Point out each leukocyte.
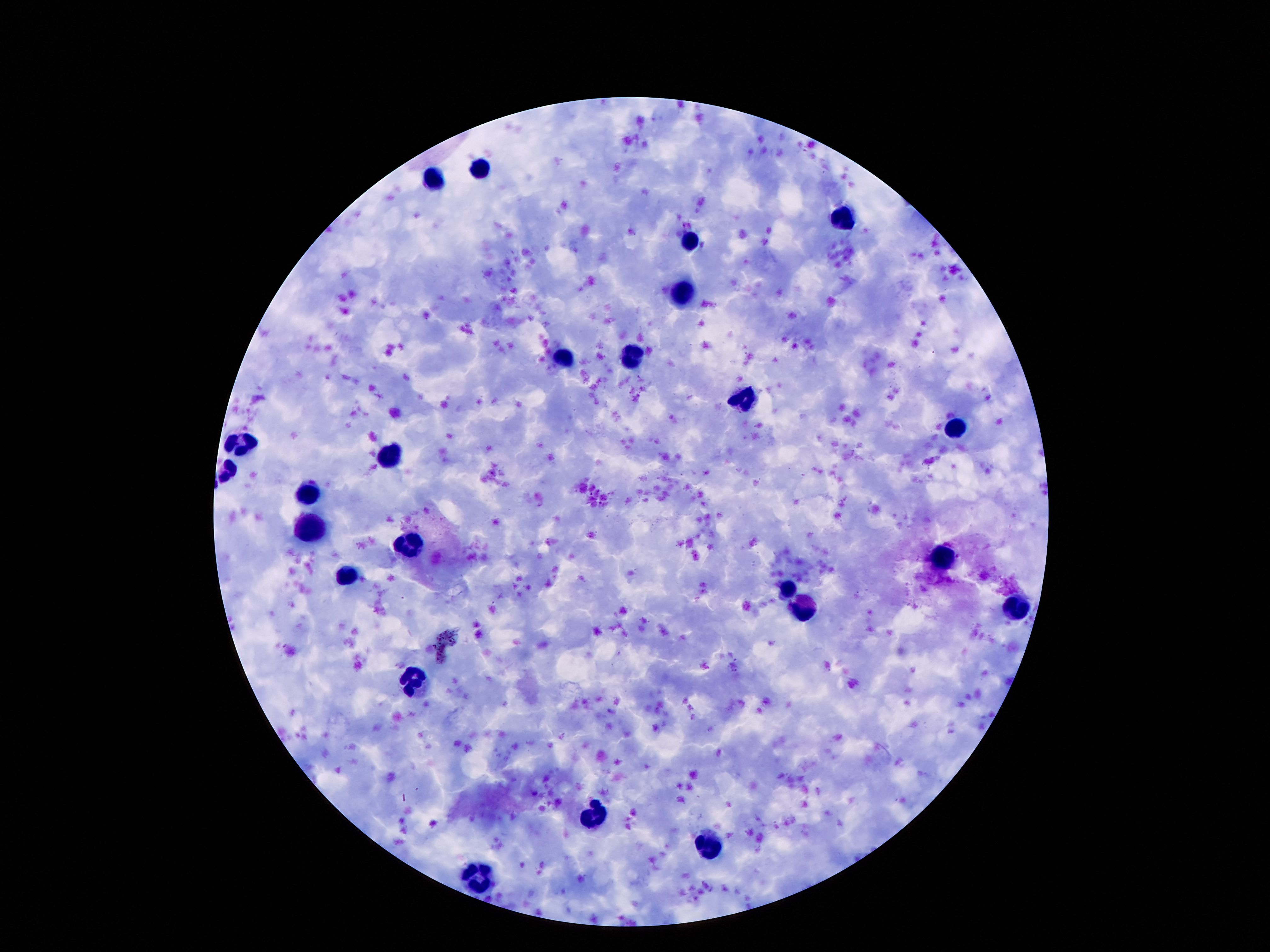
Approximate centers as [x, y] in pixels.
Leukocytes: [483, 167], [433, 181], [843, 219], [692, 241], [680, 292], [635, 355], [562, 358], [744, 400], [957, 430], [244, 444], [392, 459], [304, 494], [310, 528], [412, 544], [944, 555], [346, 576], [787, 589], [805, 607], [1018, 609], [412, 679], [592, 816], [714, 844], [481, 878].

Summary:
  - Image size: 1270×952 pixels
  - Magnification: 100x
  - Field of view: single
  - Stain: Giemsa
  - Capture: smartphone camera through the microscope eyepiece
  - Preparation: thick peripheral-blood smear
  - Patient malaria status: not infected